Classify this cell by malaria status.
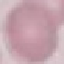
It is uninfected.

stain: Giemsa
image_type: cell patch, automatically extracted from a larger field of view and resized to 64 × 64 pixels
preparation: thin blood film
capture: smartphone through the microscope eyepiece